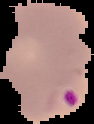 Segmented cell region on a black background. Image is 94×124 pixels. Malaria status: parasitized. From a thin blood smear.